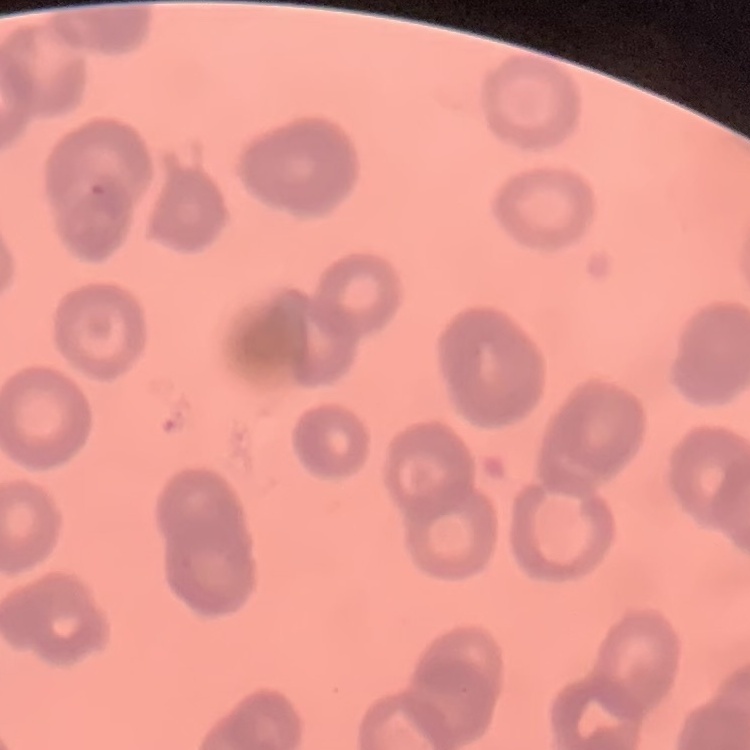
red blood cell morphology = rouleaux formation
image type = square crop of a larger photomicrograph
stain = Field's or Giemsa
preparation = thin blood smear